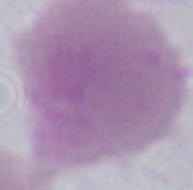
Summary:
  - Identification: erythrocyte
  - Modality: micrograph
  - Magnification: 1000x